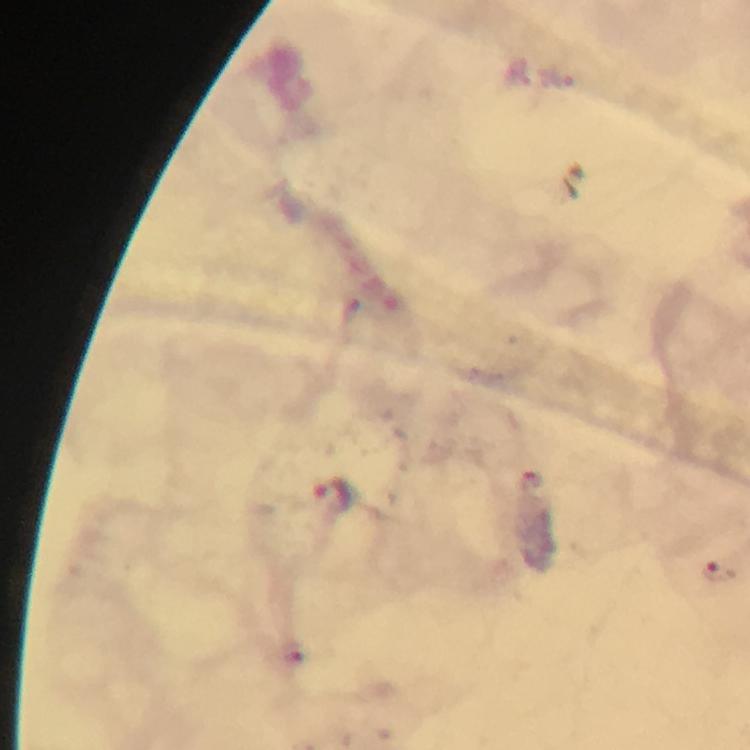

immersion_oil: used
magnification: 100x
image_size: 750×750 pixels
stain: Giemsa
malaria_parasite_locations: 'approximate object centers, in pixels from the top-left corner: (x=329, y=494), (x=719, y=569)'
preparation: thick smear
context: from a malaria diagnostic workup
capture: smartphone mounted on the microscope
cropped_from: one field of view